Identify the parasite.
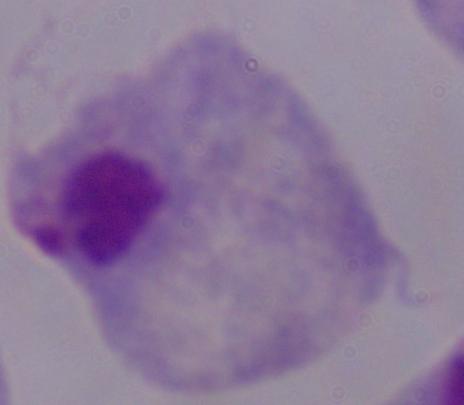

A trichomonad.

Summary:
  - Magnification: 1000x
  - Modality: photomicrograph